Point out each leukocyte.
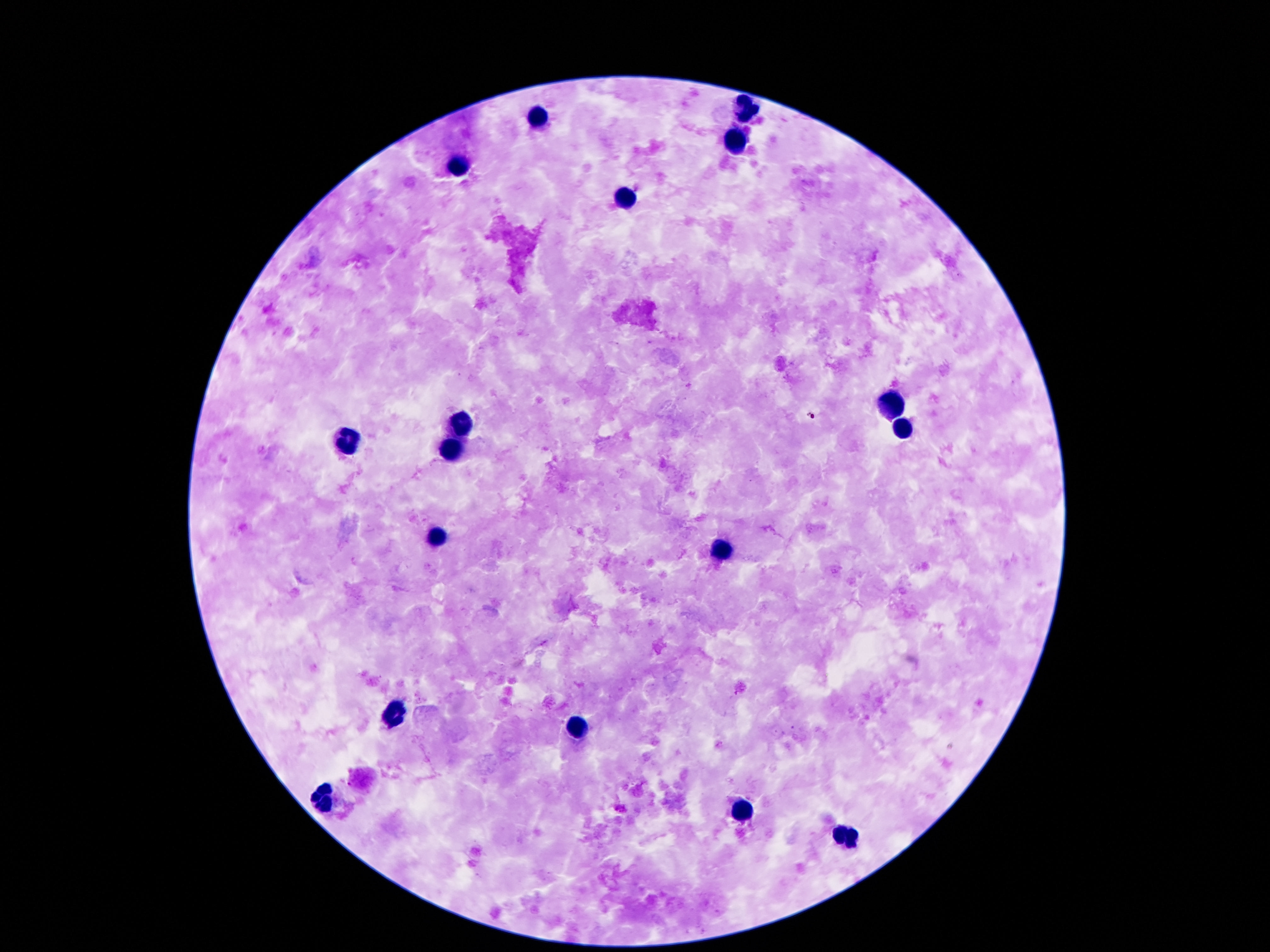
Approximate centers as [x, y] in pixels.
Leukocytes: [744, 109], [536, 116], [738, 137], [460, 170], [624, 198], [888, 406], [460, 421], [904, 429], [346, 439], [452, 452], [439, 538], [723, 549], [393, 714], [576, 727], [322, 798], [740, 811], [846, 833].

Thick blood film. Giemsa-stained preparation. 100x magnification. Image is 1270×952 pixels. Smartphone photograph taken through the microscope eyepiece. Single field of view. Patient malaria status: not infected.